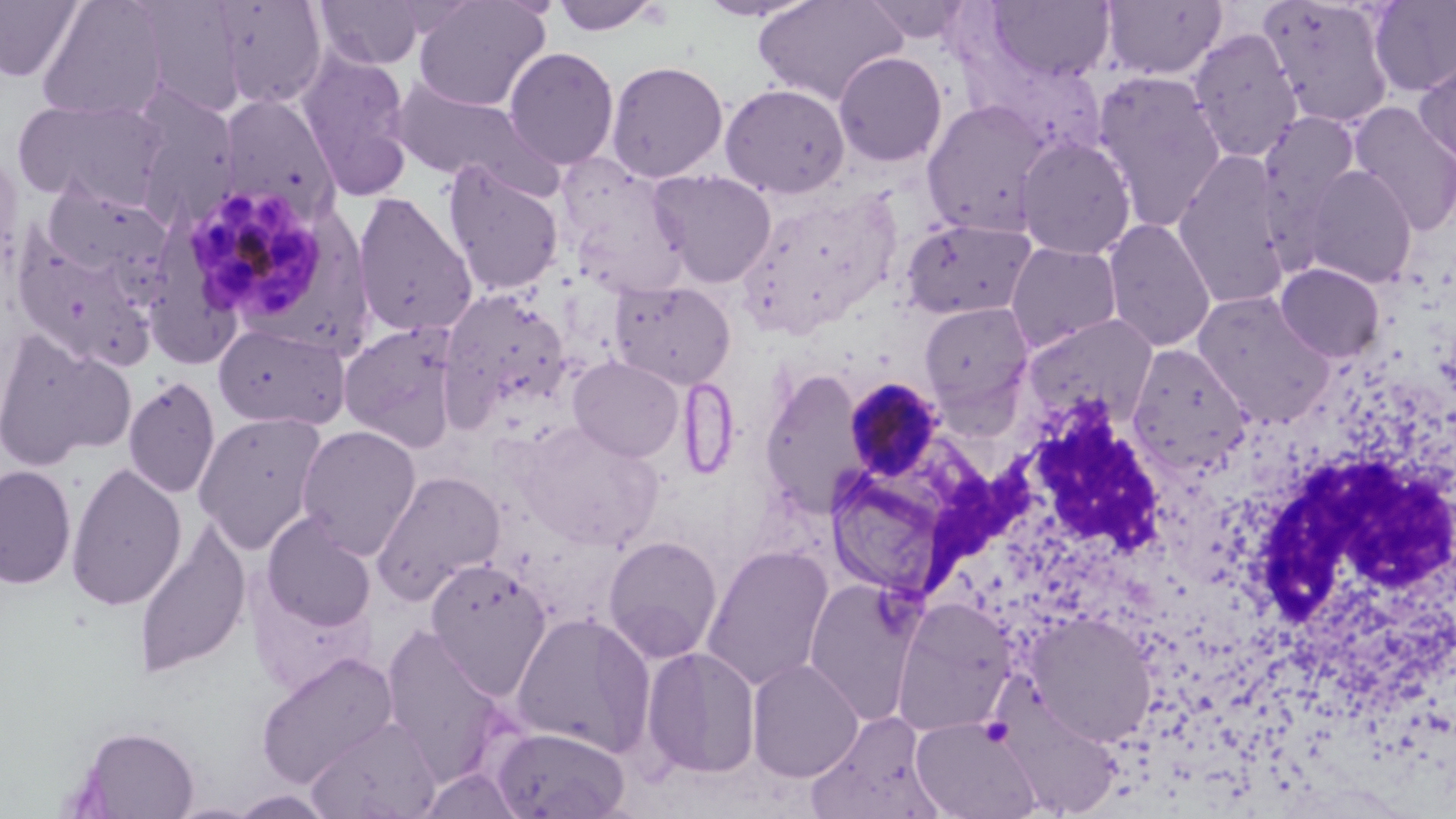
Approximate bounding boxes as named x1/y1/x2/y2 corners in pixels. Plasmodium malariae-infected red blood cell locations: (x1=194, y1=190, x2=323, y2=314), (x1=842, y1=379, x2=947, y2=482). Uninfected red blood cell locations: (x1=36, y1=0, x2=172, y2=122), (x1=412, y1=0, x2=550, y2=111), (x1=549, y1=0, x2=666, y2=36), (x1=695, y1=0, x2=819, y2=23), (x1=753, y1=0, x2=907, y2=106), (x1=862, y1=0, x2=978, y2=43), (x1=1102, y1=0, x2=1227, y2=80), (x1=1258, y1=0, x2=1395, y2=129), (x1=0, y1=1, x2=86, y2=83), (x1=124, y1=1, x2=249, y2=119), (x1=208, y1=1, x2=331, y2=111), (x1=313, y1=1, x2=429, y2=71), (x1=986, y1=1, x2=1116, y2=83), (x1=1369, y1=1, x2=1456, y2=97), (x1=1187, y1=27, x2=1303, y2=163), (x1=504, y1=46, x2=619, y2=170), (x1=295, y1=50, x2=413, y2=195), (x1=833, y1=52, x2=947, y2=167), (x1=1415, y1=54, x2=1456, y2=169), (x1=605, y1=59, x2=729, y2=183), (x1=1092, y1=72, x2=1227, y2=231), (x1=391, y1=80, x2=550, y2=193), (x1=719, y1=83, x2=850, y2=199), (x1=127, y1=89, x2=242, y2=228), (x1=217, y1=94, x2=341, y2=224), (x1=14, y1=97, x2=169, y2=210), (x1=921, y1=100, x2=1053, y2=237), (x1=1350, y1=103, x2=1456, y2=235), (x1=1260, y1=112, x2=1361, y2=215), (x1=1014, y1=135, x2=1136, y2=260), (x1=0, y1=147, x2=25, y2=284), (x1=1172, y1=153, x2=1291, y2=310), (x1=441, y1=162, x2=564, y2=296), (x1=562, y1=164, x2=691, y2=298), (x1=1298, y1=165, x2=1418, y2=288), (x1=649, y1=169, x2=776, y2=288), (x1=40, y1=181, x2=173, y2=286), (x1=740, y1=185, x2=904, y2=329), (x1=352, y1=193, x2=477, y2=339), (x1=900, y1=217, x2=1037, y2=320), (x1=150, y1=218, x2=241, y2=369), (x1=1103, y1=218, x2=1216, y2=352), (x1=8, y1=230, x2=157, y2=369), (x1=1005, y1=241, x2=1122, y2=353), (x1=1275, y1=262, x2=1385, y2=363), (x1=608, y1=280, x2=737, y2=390), (x1=440, y1=288, x2=572, y2=422), (x1=1192, y1=291, x2=1334, y2=426), (x1=919, y1=302, x2=1035, y2=414), (x1=1020, y1=314, x2=1161, y2=427), (x1=338, y1=321, x2=465, y2=453), (x1=213, y1=323, x2=351, y2=430), (x1=0, y1=330, x2=136, y2=471), (x1=1126, y1=344, x2=1253, y2=474), (x1=568, y1=356, x2=683, y2=462), (x1=760, y1=368, x2=868, y2=517), (x1=122, y1=375, x2=221, y2=499), (x1=192, y1=411, x2=328, y2=554), (x1=513, y1=421, x2=665, y2=552), (x1=296, y1=424, x2=422, y2=559), (x1=65, y1=461, x2=187, y2=612), (x1=0, y1=463, x2=78, y2=590), (x1=371, y1=470, x2=507, y2=603), (x1=261, y1=513, x2=377, y2=632), (x1=132, y1=523, x2=250, y2=679), (x1=602, y1=535, x2=723, y2=662), (x1=700, y1=544, x2=834, y2=692), (x1=425, y1=558, x2=552, y2=698), (x1=248, y1=578, x2=377, y2=697), (x1=804, y1=578, x2=921, y2=723), (x1=891, y1=598, x2=1017, y2=735), (x1=1025, y1=610, x2=1158, y2=746), (x1=511, y1=612, x2=656, y2=758), (x1=378, y1=623, x2=516, y2=787), (x1=640, y1=645, x2=762, y2=779), (x1=256, y1=652, x2=399, y2=788), (x1=746, y1=658, x2=864, y2=782), (x1=805, y1=711, x2=943, y2=819), (x1=305, y1=716, x2=442, y2=819), (x1=911, y1=717, x2=1041, y2=819), (x1=69, y1=724, x2=201, y2=818), (x1=489, y1=725, x2=631, y2=819), (x1=227, y1=789, x2=339, y2=818). White blood cell locations: (x1=925, y1=402, x2=1170, y2=597), (x1=1243, y1=452, x2=1455, y2=667). Slide-level diagnosis: Plasmodium malariae. Light microscopy. May-Grünwald-Giemsa-stained preparation. Single field of view. Captured at 1000x magnification. Thin blood smear. Image is 1456×819 pixels.